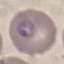
malaria status = parasitized
preparation = thin blood smear
image type = cell patch, automatically extracted from a larger field of view and resized to 64 × 64 pixels
capture = smartphone camera at the microscope eyepiece
stain = Giemsa